Name the parasite shown.
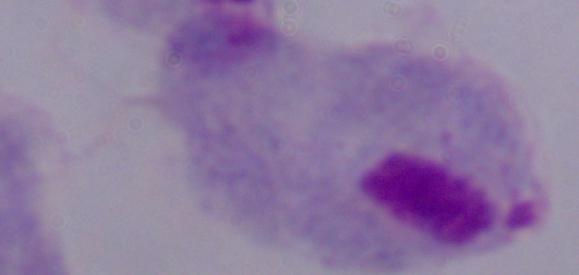

A trichomonad.

Micrograph. Captured at 1000x magnification.